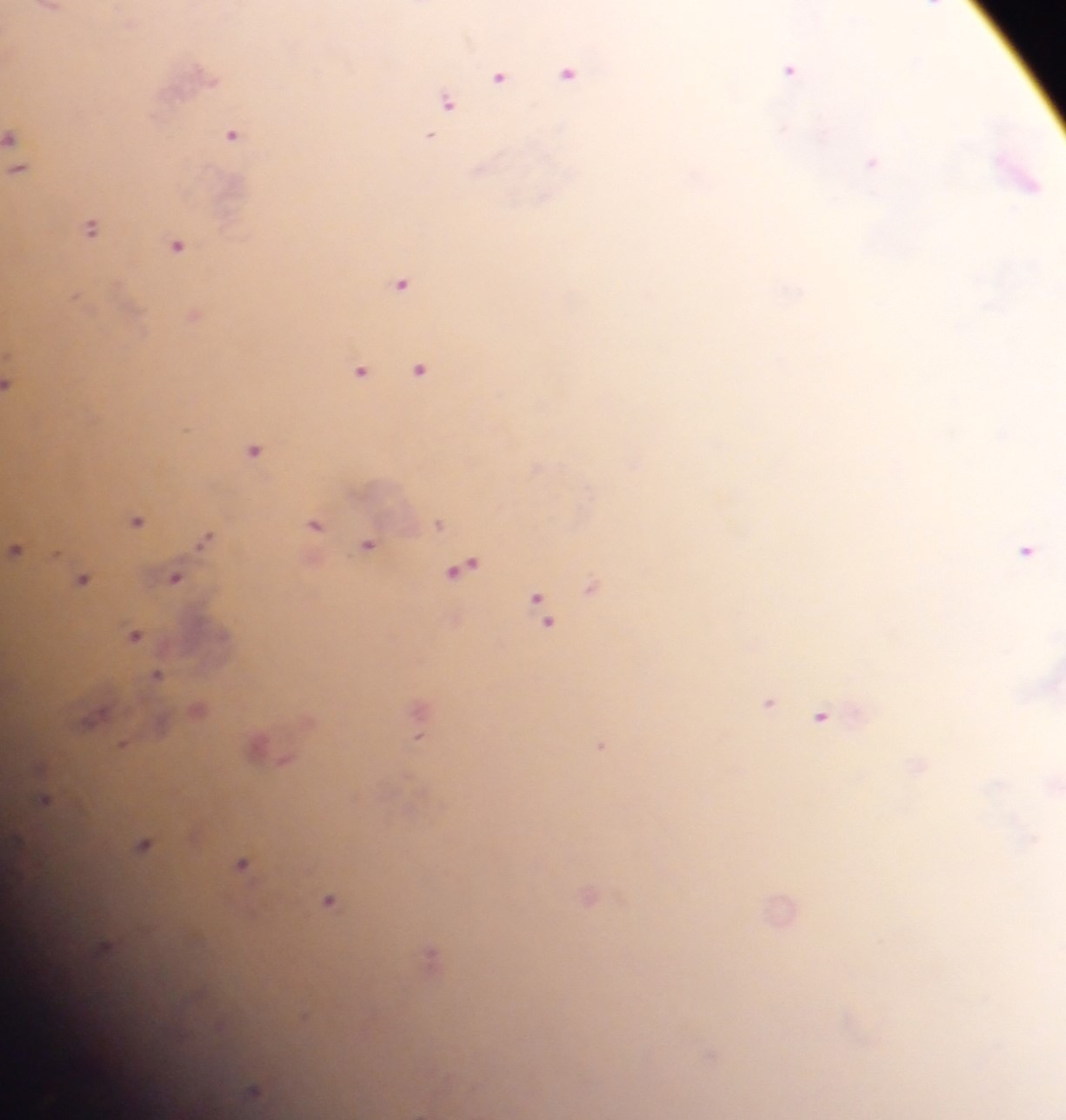 Approximate centers as x y in pixels. Malaria parasite locations: 933 5; 48 8; 789 69; 568 72; 498 76; 447 102; 231 134; 12 137; 428 137; 872 162; 17 167; 1025 180; 90 227; 176 244; 401 282; 194 314; 418 367; 359 370; 10 383; 255 449; 136 520; 315 524; 439 524; 204 538; 367 543; 16 548; 1025 549; 462 566; 175 577; 81 579; 591 586; 536 598; 544 618; 135 634; 157 675; 768 701; 196 709; 821 715; 422 716; 94 718; 419 735; 124 744; 258 744; 601 745; 45 800; 143 844; 241 864; 588 895; 328 900; 780 909; 104 950; 430 955; 254 1089. Thick blood film. Photographed through a microscope with a mobile-phone camera. Image is 1066×1120 pixels. One field of view. Sample from Ghana.